Classify this cell by malaria status.
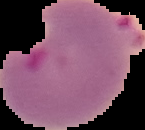
It is parasitized.

Summary:
  - Image type: segmented cell region on a black background
  - Image size: 145×130 pixels
  - Preparation: thin blood film